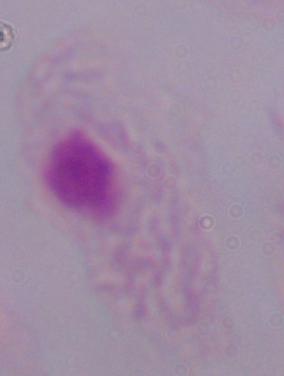
modality = photomicrograph
magnification = 1000x
identification = trichomonad